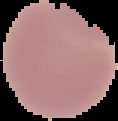

From a thin blood film. Cell region segmented out of the field of view; the surrounding area is masked to black. Image is 118×121 pixels. Result: no Plasmodium parasites seen.